State which parasite is depicted.
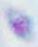

This is Toxoplasma gondii.

Photomicrograph. 1000x magnification.